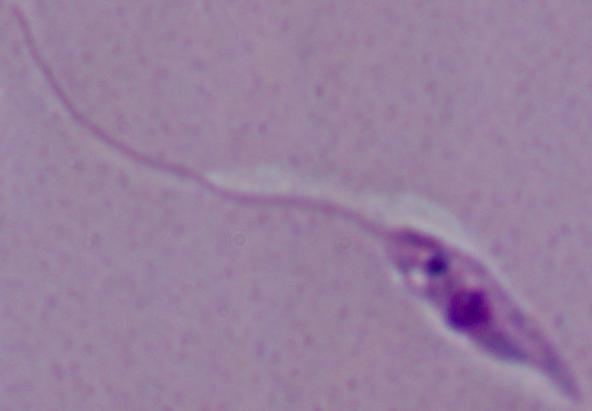

A Leishmania parasite is shown. 1000x magnification. Micrograph.